Identify the parasite.
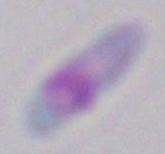

Toxoplasma gondii.

magnification = 1000x
modality = photomicrograph